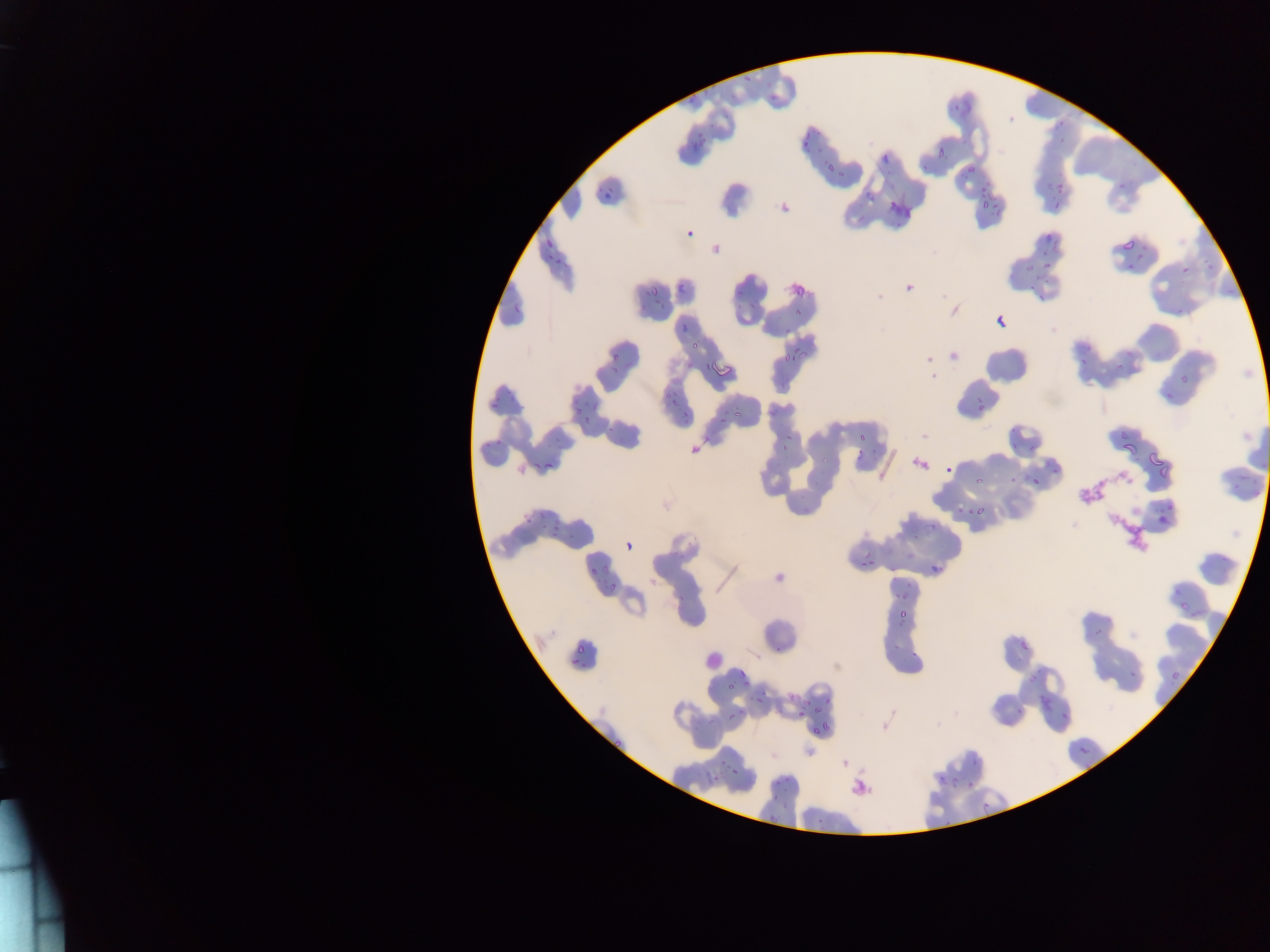

{
  "capture": "mobile-phone photograph through a microscope",
  "image_size": "1270×952 pixels",
  "country": "Ghana",
  "field_of_view": "single",
  "malaria_parasite_locations": "approximate bounding boxes as left top right bottom in pixels (subset; some below the resolvable size): 742 70 755 83; 703 79 720 95; 765 79 776 88; 686 92 698 106; 769 92 780 105; 953 103 961 111; 1057 118 1064 126; 804 124 818 143; 689 133 704 150; 801 138 812 148; 937 142 951 161; 815 144 826 158; 880 150 889 168; 967 159 978 178; 827 161 838 171; 918 164 933 175; 837 168 844 177; 1049 178 1068 200; 596 180 615 202; 1118 181 1125 189; 862 191 875 202; 979 192 987 207; 990 203 998 214; 1053 204 1062 212; 853 214 870 222; 684 224 697 239; 1047 233 1055 241; 546 239 554 248; 1051 240 1059 251; 1121 240 1133 251; 1138 243 1149 252; 1202 253 1215 274; 545 254 553 264; 1134 254 1147 260; 556 259 570 266; 1042 259 1053 269; 1025 260 1040 270; 1126 261 1137 273; 1180 265 1190 274; 1042 273 1055 284; 1029 280 1038 292; 676 283 687 293; 650 287 659 299; 736 289 745 299; 1036 290 1047 301; 654 294 664 307; 514 297 524 312; 748 299 758 310; 790 304 805 317; 996 315 1005 325; 682 319 692 333; 783 328 792 336; 1083 335 1094 354; 689 341 701 349; 784 346 809 362; 611 351 619 362; 1079 354 1089 367; 1111 356 1133 369; 685 359 694 368; 703 360 714 373; 622 362 636 368; 605 364 618 378; 1180 372 1193 385; 507 376 521 403; 663 383 682 400; 1164 392 1177 402; 488 395 501 410; 973 396 989 412; 667 398 678 409; 587 399 597 409; 571 406 585 416; 734 407 743 418; 768 407 781 421; 681 408 690 422; 583 414 593 431; 720 414 728 422; 605 419 616 436; 1010 425 1018 434; 859 428 869 440; 1119 428 1132 446; 496 436 504 446; 552 436 560 441; 780 438 792 451; 485 441 491 450; 1009 442 1017 452; 1122 443 1141 457; 556 444 566 452; 1029 444 1037 454; 853 447 867 464; 1150 448 1158 467; 530 455 541 471; 822 455 830 466; 1158 456 1174 481; 543 459 558 469; 944 465 953 474; 1052 467 1061 476; 1237 470 1251 482; 1031 472 1041 490; 973 476 982 485; 1009 478 1019 486; 1230 485 1241 494; 1253 493 1263 503; 1164 497 1176 511; 956 503 967 514; 802 504 813 516; 970 505 983 517; 538 511 546 520; 1155 511 1168 529; 525 513 532 525; 549 513 566 540; 910 521 921 546; 625 539 636 550; 1220 554 1230 566; 860 558 878 570; 601 560 612 577; 928 562 944 574; 589 567 599 577; 890 567 899 574; 602 584 620 598; 677 591 687 606; 893 592 908 601; 1181 601 1192 612; 898 606 909 618; 897 620 908 628; 1093 629 1103 638; 893 640 904 650; 1021 640 1032 650; 571 644 592 656; 775 646 783 657; 909 651 920 659; 570 659 580 667; 1169 667 1180 681; 738 668 746 677; 738 670 748 681; 1027 672 1041 684; 1126 672 1140 682; 743 679 754 691; 727 681 738 693; 824 692 836 708; 788 693 797 704; 1040 697 1050 709; 754 698 765 705; 802 698 811 706; 738 706 747 716; 811 706 821 719; 797 707 807 717; 1016 710 1025 717; 727 712 736 721; 1061 713 1070 723; 822 718 834 739; 810 725 821 735; 613 736 627 751; 1079 746 1089 755; 716 751 728 769; 711 771 728 789; 783 774 795 782; 772 778 781 787; 967 781 975 790; 816 817 825 827 | approximate x y pixel centers of objects too small to bound: 983 188; 543 528; 554 633",
  "preparation": "thin blood film",
  "leukocyte_locations": "approximate bounding boxes as left top right bottom in pixels: 701 648 724 672"
}